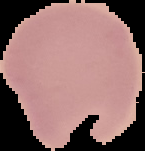
{
  "malaria_status": "uninfected",
  "image_type": "segmented cell region with the area outside set to black",
  "preparation": "thin blood film",
  "image_size": "145×151 pixels"
}